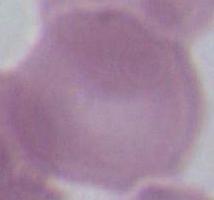

magnification: 1000x
identification: erythrocyte
modality: micrograph